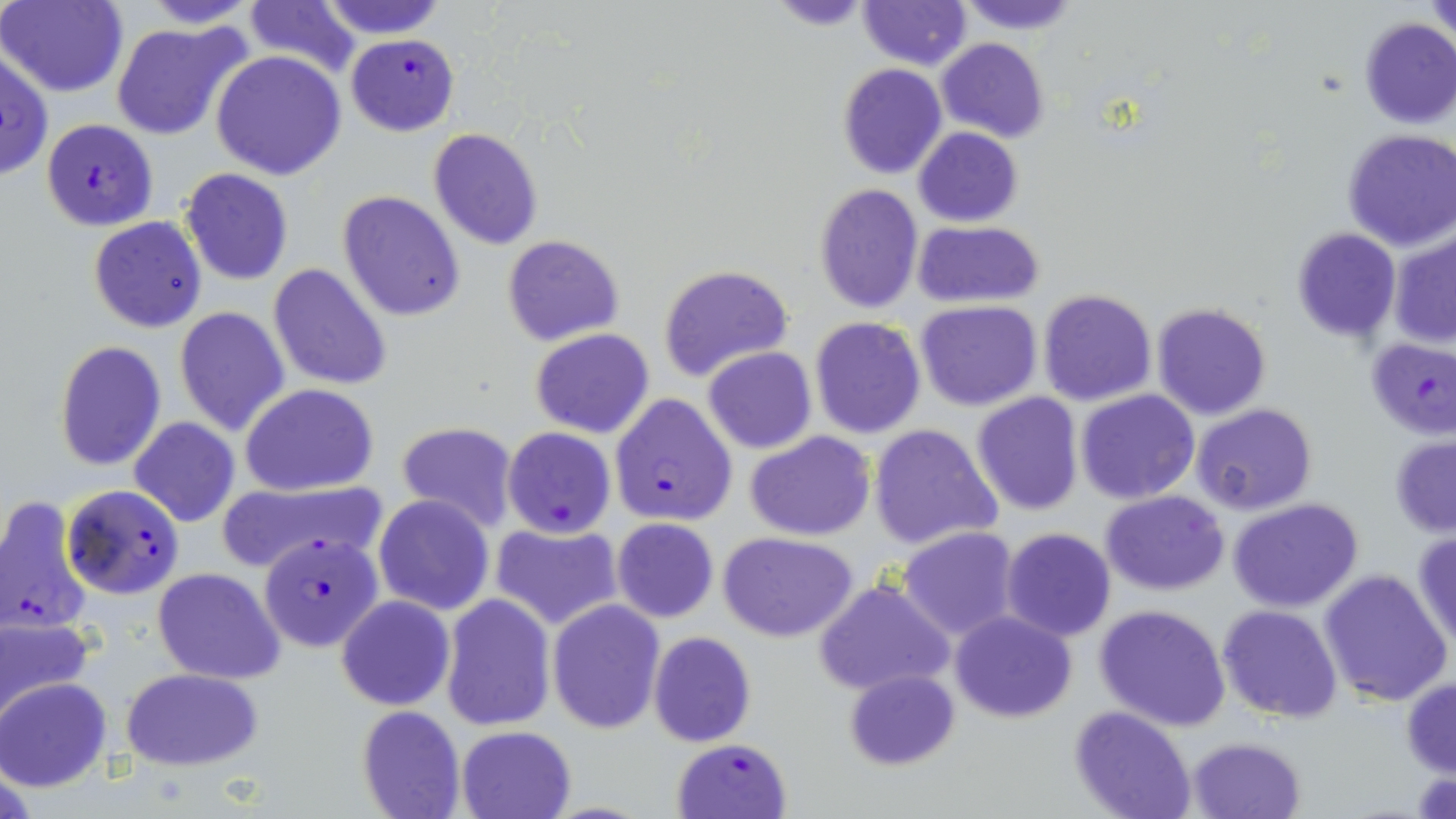 Approximate bounding boxes as (x1, y1, x2, y2) in pixels. Uninfected red blood cell locations: (2, 0, 127, 97), (140, 0, 262, 27), (318, 0, 448, 39), (859, 0, 971, 69), (954, 0, 1081, 35), (1426, 0, 1456, 40), (243, 1, 363, 81), (1358, 17, 1456, 128), (111, 21, 249, 142), (936, 37, 1050, 142), (0, 48, 52, 182), (211, 50, 346, 181), (837, 63, 947, 178), (428, 127, 544, 249), (913, 127, 1022, 227), (1341, 130, 1456, 250), (179, 168, 294, 285), (813, 183, 924, 315), (338, 190, 466, 322), (88, 216, 207, 334), (911, 222, 1043, 307), (1290, 227, 1402, 345), (1389, 228, 1456, 350), (502, 234, 625, 347), (269, 263, 393, 393), (658, 264, 794, 384), (1037, 288, 1158, 407), (915, 300, 1041, 411), (1151, 302, 1272, 419), (173, 307, 289, 437), (809, 316, 927, 439), (530, 328, 654, 439), (54, 339, 166, 469), (703, 346, 817, 454), (241, 383, 378, 495), (1076, 389, 1200, 504), (971, 392, 1084, 515), (1191, 403, 1317, 516), (128, 417, 241, 528), (402, 420, 525, 530), (867, 423, 1003, 551), (744, 431, 877, 542), (1389, 436, 1456, 537), (217, 479, 381, 577), (1101, 490, 1229, 595), (373, 494, 495, 617), (1227, 498, 1364, 612), (611, 518, 720, 623), (490, 522, 621, 630), (898, 526, 1021, 640), (1412, 527, 1456, 649), (1001, 528, 1116, 643), (719, 532, 859, 642), (152, 567, 285, 684), (1318, 568, 1453, 706), (811, 578, 955, 699), (336, 594, 454, 711), (441, 594, 557, 732), (547, 600, 665, 734), (1093, 603, 1231, 732), (1218, 604, 1343, 722), (950, 611, 1077, 723), (0, 613, 94, 723), (649, 631, 756, 746), (119, 667, 265, 769), (843, 668, 961, 770), (1401, 676, 1456, 778), (0, 678, 111, 791), (356, 705, 466, 818), (1069, 705, 1197, 819), (456, 724, 577, 819), (1187, 737, 1308, 819). Plasmodium falciparum-infected red blood cell locations: (347, 33, 459, 137), (40, 118, 159, 231), (1362, 335, 1456, 439), (610, 394, 737, 526), (502, 427, 616, 537), (62, 484, 185, 599), (0, 496, 92, 636), (260, 534, 382, 651), (672, 738, 792, 819). Slide-level diagnosis: Plasmodium falciparum. One field of a larger specimen. Optical microscopy. 1000x magnification. Thin blood film. May-Grünwald-Giemsa stain. Image is 1456×819 pixels.